Outline each blood parasite and name the species.
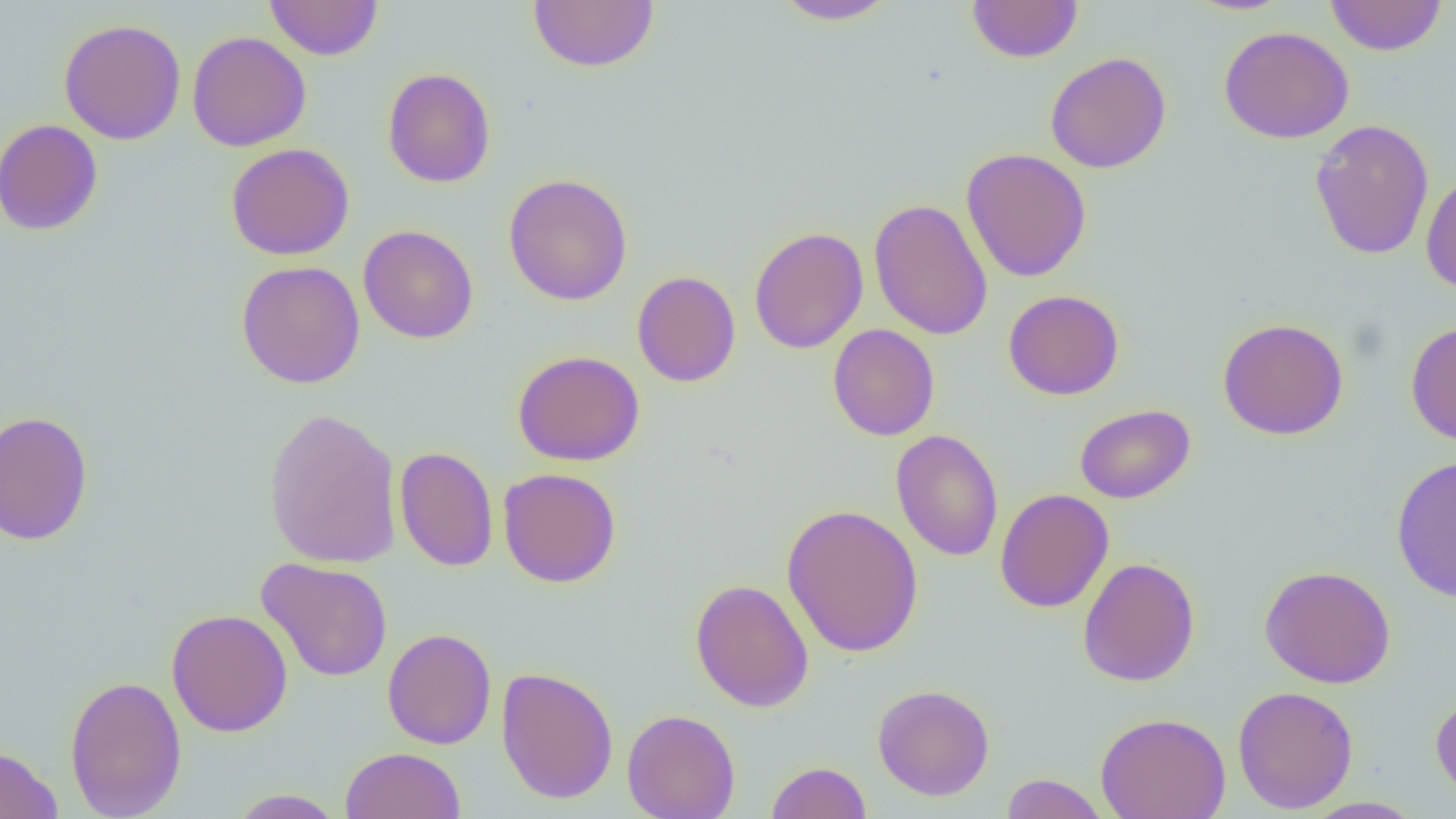

No blood parasites seen.

slide-level diagnosis = negative for blood parasites
modality = optical microscopy
magnification = 1000x
preparation = thin blood smear
uninfected red blood cell locations = approximate bounding boxes as [x1, y1, x2, y2] in pixels: [264, 0, 383, 61], [771, 0, 901, 25], [966, 0, 1084, 63], [1325, 0, 1447, 56], [528, 1, 659, 72], [58, 18, 186, 145], [1219, 26, 1355, 144], [187, 31, 312, 152], [1045, 51, 1172, 173], [382, 67, 496, 188], [1309, 118, 1434, 260], [0, 119, 103, 237], [225, 142, 355, 261], [960, 148, 1092, 283], [1420, 169, 1456, 295], [503, 173, 633, 306], [868, 198, 993, 340], [358, 224, 479, 343], [749, 226, 869, 355], [236, 260, 366, 388], [631, 270, 741, 388], [1003, 289, 1125, 401], [1217, 317, 1349, 440], [1405, 320, 1456, 446], [827, 324, 940, 441], [512, 350, 645, 466], [1074, 403, 1195, 504], [263, 407, 403, 569], [1, 410, 95, 545], [890, 429, 1004, 562], [394, 446, 499, 572], [1390, 455, 1456, 603], [498, 468, 622, 588], [995, 488, 1113, 613], [781, 504, 924, 659], [1077, 556, 1201, 687], [256, 557, 394, 683], [1259, 565, 1396, 689], [689, 578, 814, 713], [166, 609, 293, 737], [382, 628, 496, 749], [496, 666, 618, 804], [64, 674, 187, 819], [872, 684, 994, 801], [1232, 685, 1358, 814], [1430, 689, 1456, 803], [622, 709, 740, 819], [1095, 712, 1231, 819], [0, 744, 64, 819], [340, 747, 466, 819], [765, 761, 872, 819], [1000, 773, 1110, 818], [228, 789, 345, 818], [1300, 796, 1426, 818]
image size = 1456×819 pixels
field of view = single